Assess this cell for malaria.
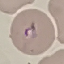
It is parasitized.

image type = cell patch, automatically extracted from a larger field of view and resized to 64 × 64 pixels
preparation = thin smear
stain = Giemsa
capture = smartphone camera at the microscope eyepiece